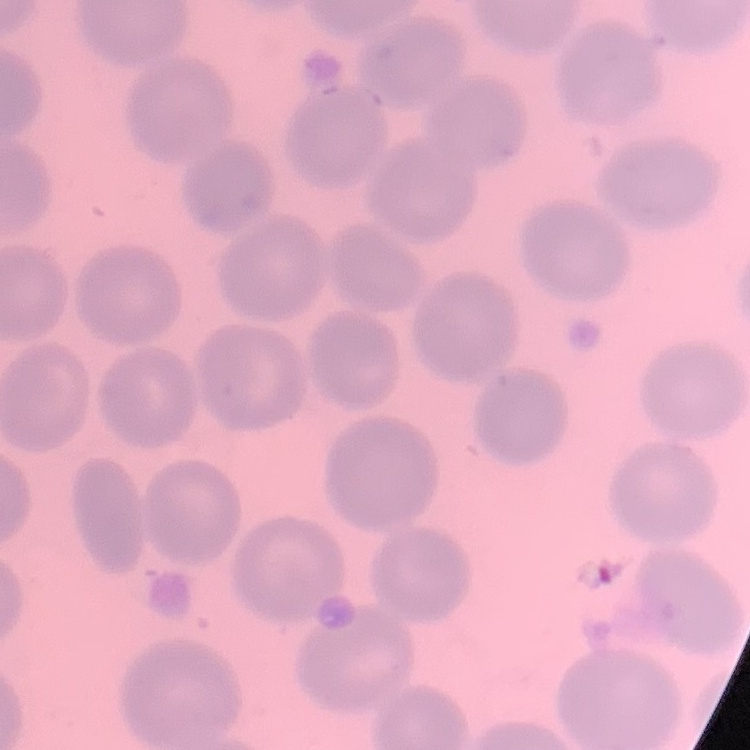
Summary:
  - Erythrocyte morphology: no rouleaux formation
  - Preparation: thin blood smear
  - Image type: square crop of a larger photomicrograph
  - Stain: Field's or Giemsa